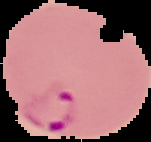

{
  "image_size": "151×142 pixels",
  "image_type": "segmented cell region on a black background",
  "result": "Plasmodium parasites detected",
  "preparation": "thin blood smear"
}